Locate every Plasmodium vivax-infected red blood cell.
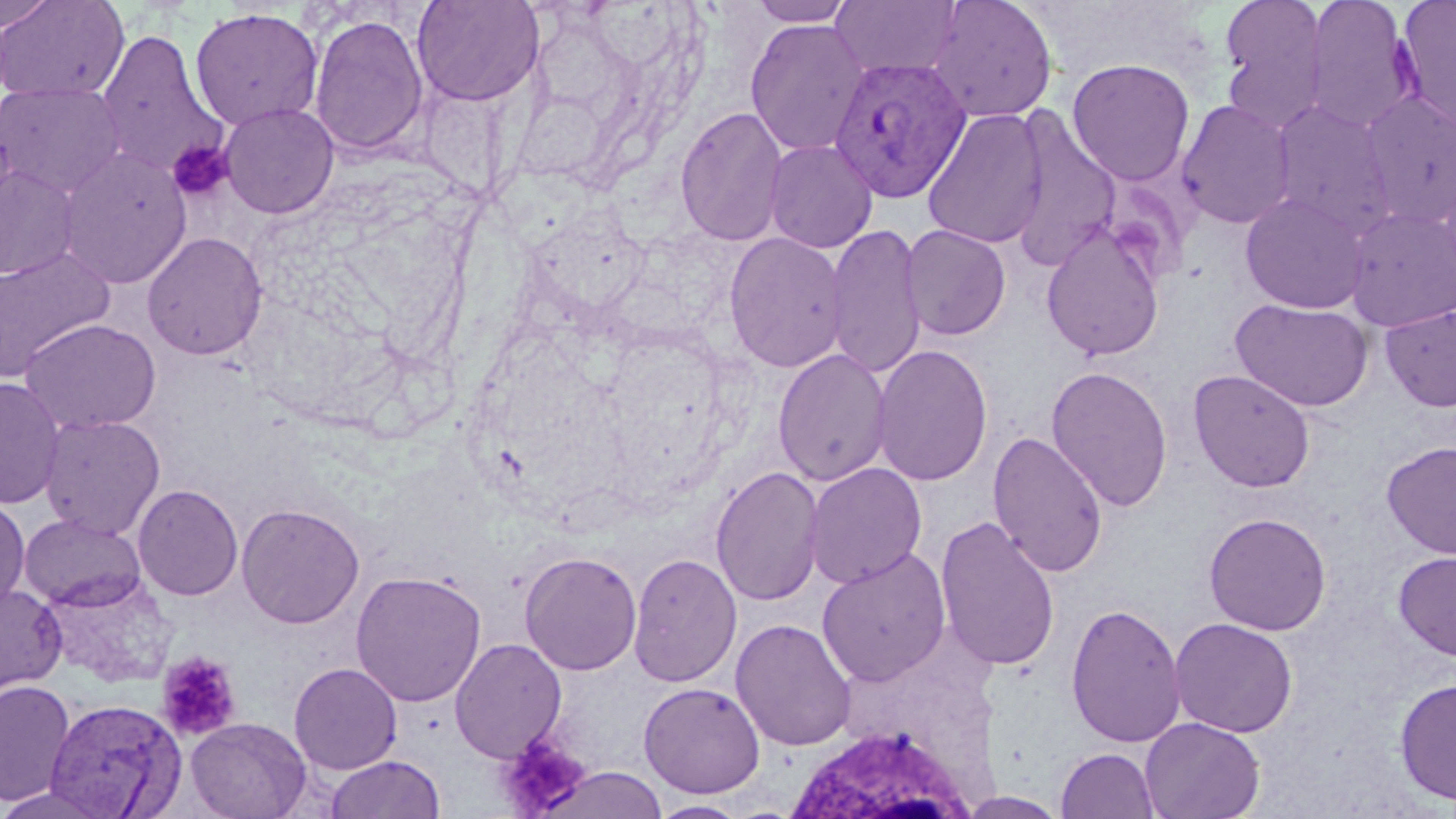

Approximate bounding boxes as [x1, y1, x2, y2] in pixels.
Plasmodium vivax-infected red blood cells: [829, 56, 970, 202].

White blood cell locations: [780, 724, 979, 819]. Platelet locations: [167, 139, 234, 202], [156, 650, 241, 740], [495, 735, 590, 818]. Uninfected red blood cell locations: [0, 0, 129, 103], [0, 0, 59, 33], [411, 0, 544, 107], [747, 0, 856, 26], [830, 0, 963, 80], [926, 0, 1058, 123], [1219, 0, 1330, 129], [1303, 0, 1416, 132], [1395, 0, 1456, 133], [189, 7, 324, 130], [309, 14, 429, 157], [744, 18, 870, 156], [95, 29, 226, 180], [1067, 58, 1195, 185], [0, 82, 126, 198], [1360, 91, 1456, 229], [1177, 100, 1296, 229], [1271, 101, 1397, 237], [217, 103, 339, 219], [676, 105, 789, 247], [922, 107, 1049, 249], [1008, 113, 1121, 271], [764, 139, 878, 253], [56, 147, 192, 289], [0, 164, 81, 281], [1239, 193, 1369, 314], [1344, 206, 1456, 331], [825, 223, 927, 381], [900, 224, 1011, 340], [1041, 226, 1166, 362], [142, 232, 267, 360], [723, 232, 848, 373], [0, 246, 114, 381], [1231, 298, 1373, 412], [1380, 305, 1456, 412], [20, 319, 161, 434], [871, 344, 993, 487], [773, 348, 892, 487], [1046, 365, 1173, 512], [1188, 368, 1316, 493], [0, 377, 66, 509], [39, 414, 165, 539], [988, 430, 1109, 578], [1380, 441, 1456, 558], [805, 462, 928, 589], [710, 465, 825, 607], [133, 484, 243, 601], [0, 498, 30, 609], [236, 502, 364, 629], [1203, 512, 1332, 636], [19, 514, 146, 610], [934, 516, 1060, 672], [816, 548, 951, 687], [519, 550, 642, 675], [1392, 550, 1456, 661], [628, 552, 742, 687], [350, 569, 487, 707], [0, 583, 66, 695], [1065, 602, 1186, 748], [1169, 617, 1298, 738], [731, 618, 857, 752], [449, 638, 567, 762], [289, 662, 403, 775], [1394, 677, 1456, 807], [0, 680, 76, 807], [638, 682, 766, 798], [44, 698, 186, 818], [185, 717, 311, 819], [1140, 717, 1265, 819], [1056, 748, 1160, 819], [324, 754, 446, 819], [539, 765, 668, 819], [0, 783, 122, 819], [961, 792, 1067, 818], [648, 800, 750, 818]. Slide-level diagnosis: Plasmodium vivax. Light microscopy. Captured at 1000x magnification. May-Grünwald-Giemsa stain. Thin blood film. Image is 1456×819 pixels. Single field of view.